Name the parasite shown.
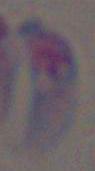
This is Toxoplasma gondii.

Captured at 1000x magnification. Micrograph.